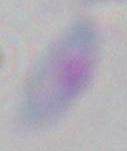

{
  "modality": "micrograph",
  "identification": "Toxoplasma gondii",
  "magnification": "1000x"
}